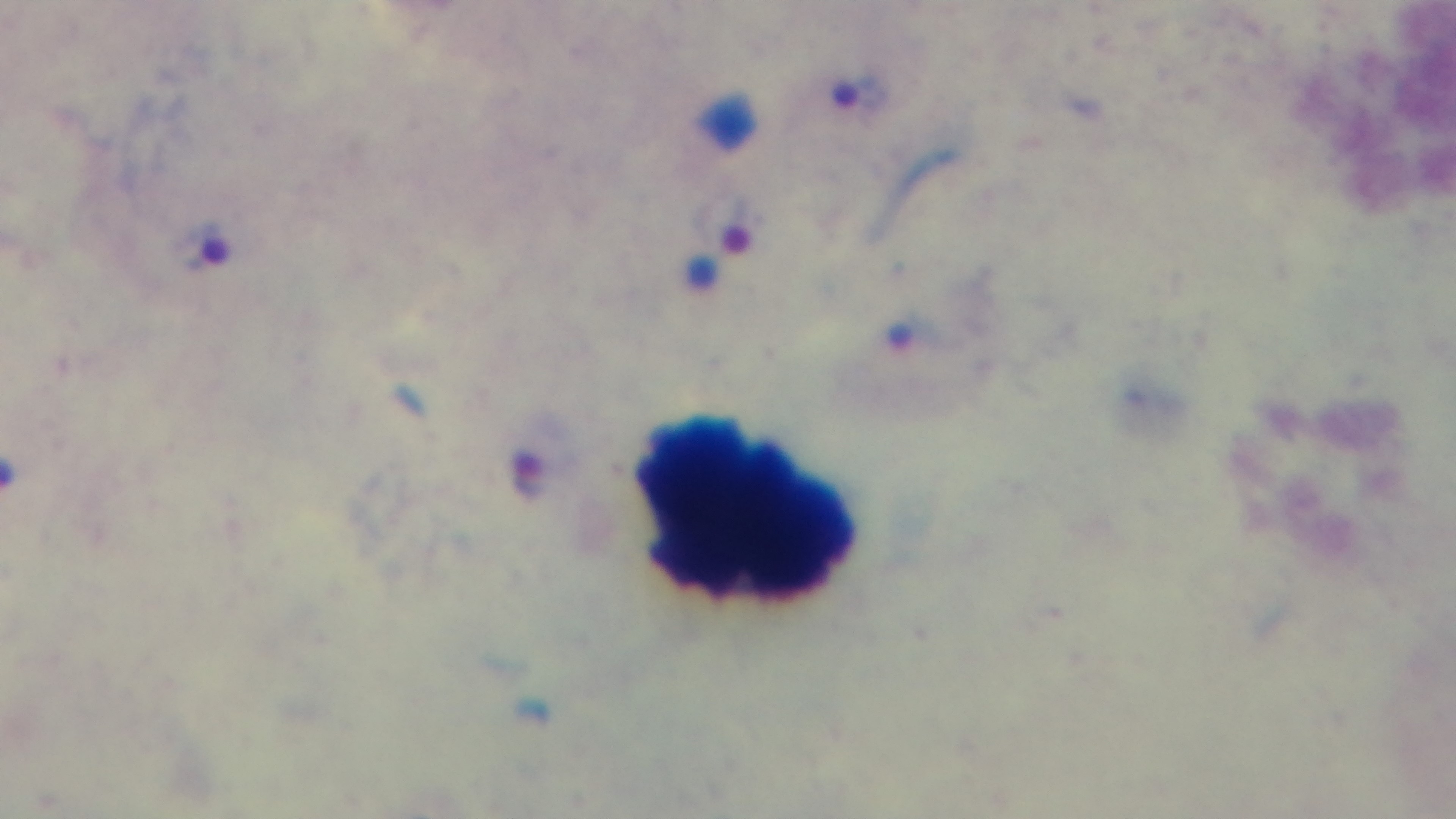

Summary:
  - Modality: light microscopy
  - Preparation: thick blood film
  - Capture: mounted 4K digital camera
  - Objective: 100x oil immersion
  - Stain: Giemsa
  - Field of view: one from the slide
  - Malaria status: positive